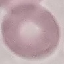
Summary:
  - Malaria status: uninfected
  - Capture: smartphone camera at the microscope eyepiece
  - Image type: cell patch, automatically extracted from a larger field of view and resized to 64 × 64 pixels
  - Preparation: thin blood film
  - Stain: Giemsa